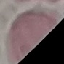
malaria status = uninfected
capture = smartphone camera at the microscope eyepiece
preparation = thin blood smear
stain = Giemsa
image type = cell patch, automatically extracted from a larger field of view and resized to 64 × 64 pixels